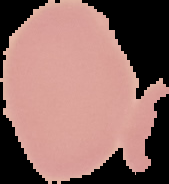
Image is 169×184 pixels. Malaria status: uninfected. From a thin blood smear. Cell region segmented out of the field of view; the surrounding area is masked to black.